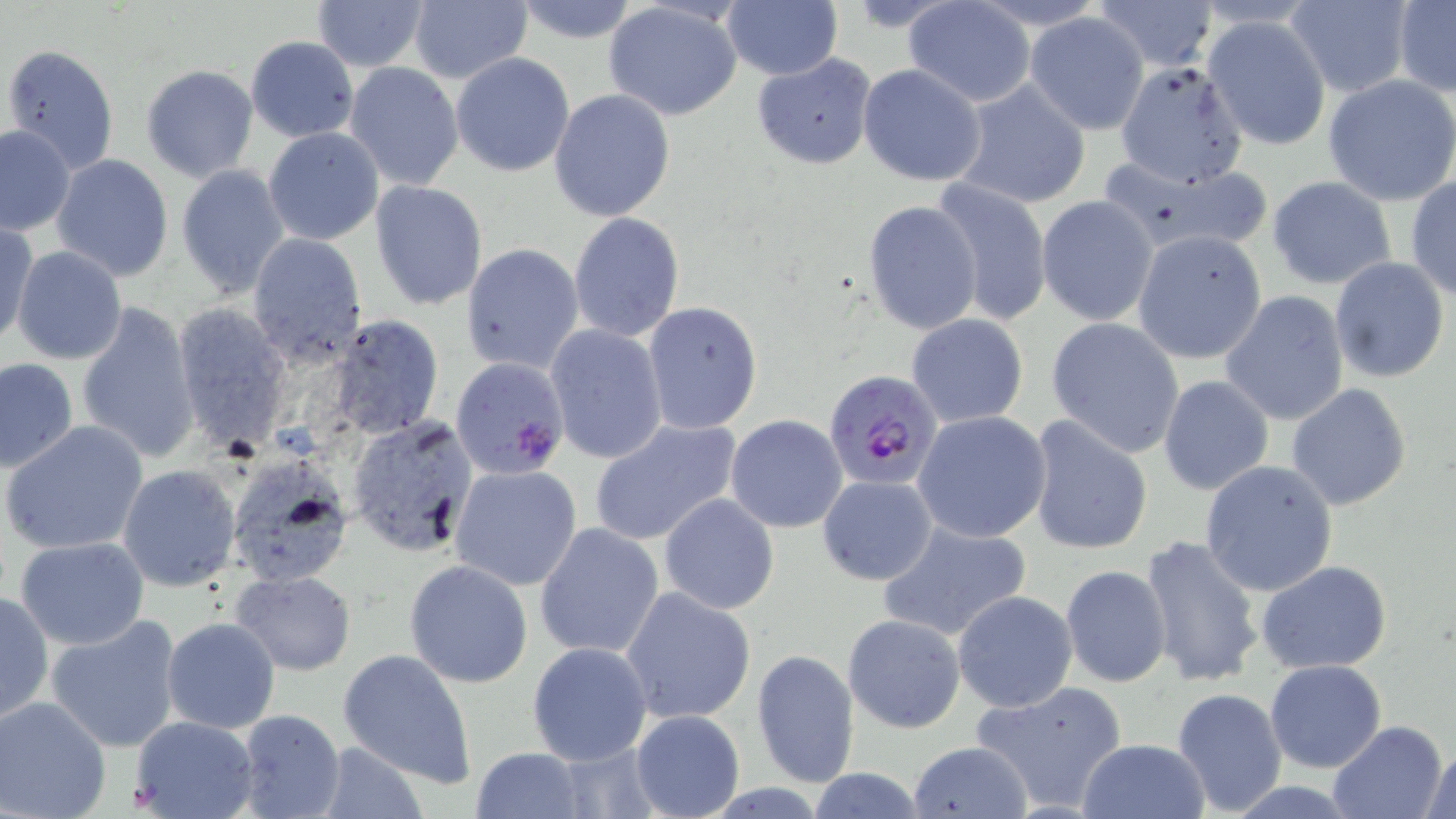

slide_level_diagnosis: Plasmodium falciparum
uninfected_red_blood_cell_locations: 'approximate bounding boxes as (x1,y1)-(x2,y2) corner pairs in pixels: (309,0)-(431,73), (511,0)-(641,45), (1096,0)-(1218,71), (405,1)-(531,86), (605,1)-(743,122), (902,1)-(1036,107), (1393,1)-(1456,96), (1283,2)-(1411,98), (721,3)-(844,81), (1024,11)-(1151,134), (1202,14)-(1332,152), (245,35)-(360,143), (4,44)-(119,173), (450,51)-(575,177), (751,53)-(878,169), (343,61)-(465,193), (140,63)-(260,182), (858,64)-(986,187), (1105,64)-(1247,187), (1323,75)-(1456,206), (954,79)-(1092,210), (550,89)-(675,223), (0,123)-(74,234), (263,127)-(383,245), (51,153)-(175,282), (1095,154)-(1274,257), (176,164)-(290,298), (1267,176)-(1397,289), (1406,178)-(1456,301), (931,180)-(1052,329), (370,181)-(489,308), (1036,194)-(1159,326), (1296,197)-(1435,345), (862,199)-(983,335), (567,211)-(685,342), (2,218)-(37,348), (1133,230)-(1269,364), (247,233)-(368,367), (461,242)-(584,374), (11,248)-(126,365), (1329,257)-(1449,385), (1218,290)-(1349,425), (640,300)-(763,433), (76,301)-(201,466), (170,302)-(293,449), (328,315)-(443,439), (906,315)-(1029,428), (1047,317)-(1185,458), (545,325)-(670,465), (0,358)-(79,473), (1158,375)-(1275,495), (1286,382)-(1412,510), (913,411)-(1055,544), (346,415)-(480,558), (725,415)-(848,533), (1025,416)-(1154,557), (588,417)-(743,546), (3,420)-(149,556), (233,453)-(358,594), (1199,460)-(1338,597), (451,464)-(581,591), (117,465)-(241,592), (817,475)-(938,587), (659,494)-(780,614), (878,518)-(1032,643), (534,521)-(665,659), (1137,534)-(1266,689), (14,538)-(151,650), (404,559)-(534,688), (1257,562)-(1391,674), (1060,564)-(1171,687), (232,570)-(356,675), (620,586)-(756,725), (952,590)-(1078,712), (0,591)-(53,725), (45,614)-(184,752), (843,614)-(964,733), (161,617)-(281,735), (526,641)-(654,766), (751,648)-(860,789), (339,650)-(477,786), (1264,659)-(1386,773), (970,681)-(1129,811), (1171,687)-(1288,814), (0,696)-(112,819), (629,709)-(745,819), (233,710)-(345,819), (129,715)-(258,819), (1326,720)-(1448,819), (1077,738)-(1210,819), (908,740)-(1031,818), (313,742)-(431,818), (1422,744)-(1455,819), (471,747)-(586,819), (801,768)-(932,818)'
stain: May-Grünwald-Giemsa
preparation: thin blood film
plasmodium_falciparum_infected_red_blood_cell_locations: 'approximate bounding boxes as (x1,y1)-(x2,y2) corner pairs in pixels: (451,358)-(572,481), (823,371)-(943,490)'
modality: optical microscopy
field_of_view: one of a larger specimen
magnification: 1000x
image_size: 1456×819 pixels